Give the preparation type.
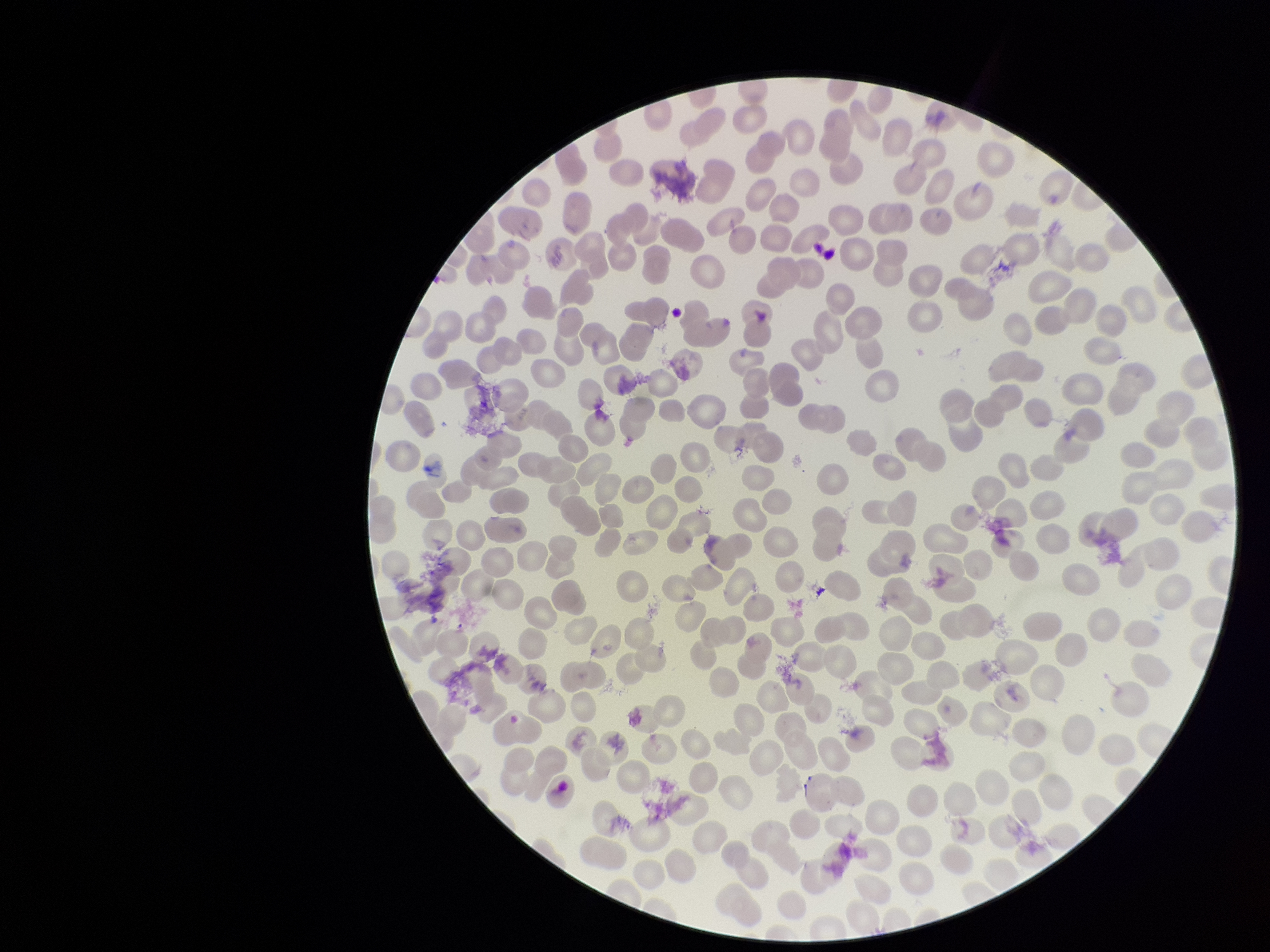
It is a thin blood smear.

Summary:
  - Red blood cell count: 258
  - Patient malaria status: positive
  - Capture: smartphone photograph through the microscope eyepiece
  - Parasitized red blood cells: none detected
  - Parasitized red blood cell count: 0
  - Field of view: one from this slide
  - Species reported for this patient: Plasmodium falciparum
  - Image size: 1270×952 pixels
  - Stain: Giemsa